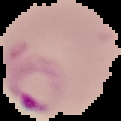

image_type: segmented cell region with the area outside set to black
preparation: thin blood film
malaria_status: parasitized
image_size: 121×121 pixels